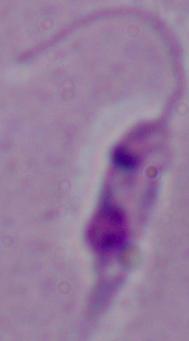

magnification = 1000x
identification = Leishmania
modality = micrograph